Report the malaria status of this cell.
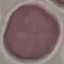

It is uninfected.

Automatically extracted cell patch, resized to 64 × 64 pixels. Thin smear of blood. Giemsa stain. Acquired by smartphone through the microscope eyepiece.